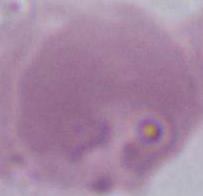
A red blood cell is seen. Micrograph. Captured at 1000x magnification.